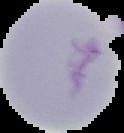
Cell region segmented out of the field of view; the surrounding area is masked to black. Image is 124×133 pixels. Result: no Plasmodium parasites seen. From a thin blood smear.